Assess the morphology of the erythrocytes.
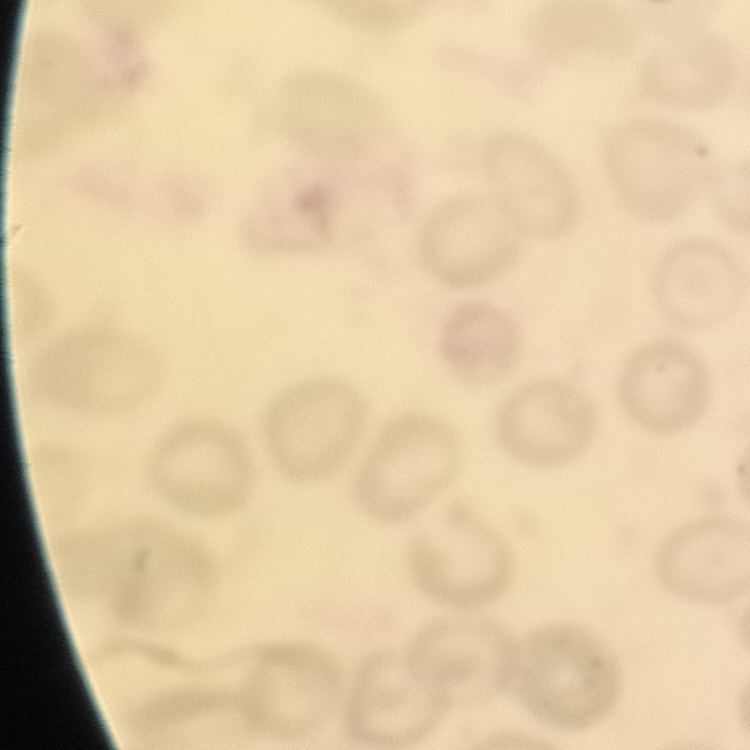

They show no rouleaux formation.

Thin peripheral smear. Square crop of a larger photomicrograph. Stained with either Field's or Giemsa.